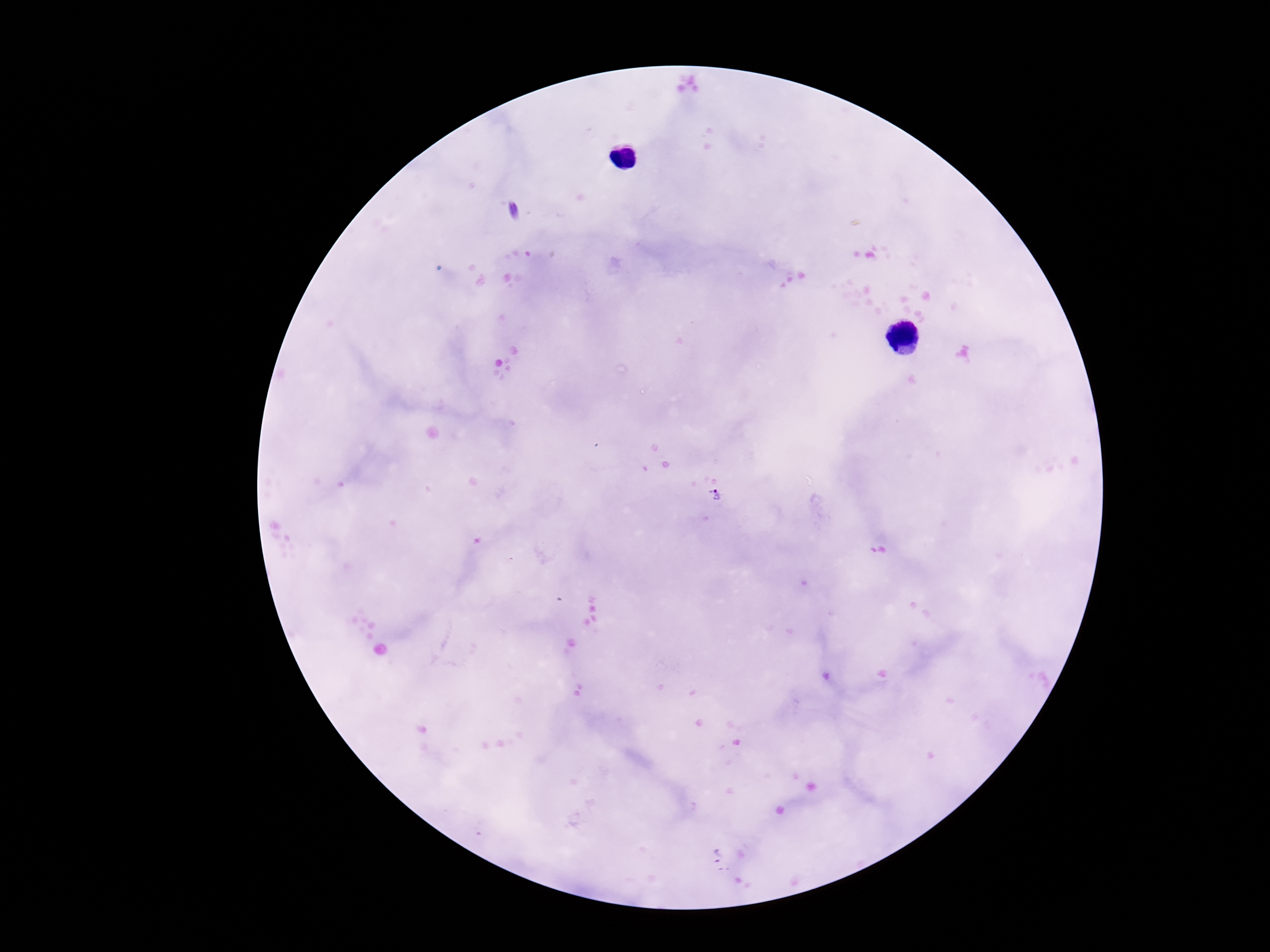 Approximate centers as (x, y) in pixels. Plasmodium parasite locations: (717, 495). 100x magnification. Image is 1270×952 pixels. Giemsa-stained preparation. Photographed through the microscope eyepiece with a smartphone camera. Patient malaria status: positive. One field from this slide. Thick blood film.